Classify this cell by malaria status.
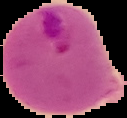
It is parasitized.

preparation = thin blood smear
image size = 127×118 pixels
image type = segmented cell region on a black background